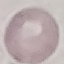 Malaria status: uninfected. Cell patch, automatically extracted from a larger field of view and resized to 64 × 64 pixels. Acquired by smartphone through the microscope eyepiece. Thin blood film. Giemsa-stained preparation.